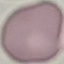 Malaria status: uninfected. Thin blood smear. Giemsa stain. Automatically extracted cell patch, resized to 64 × 64 pixels. Photographed with a smartphone camera at the microscope eyepiece.